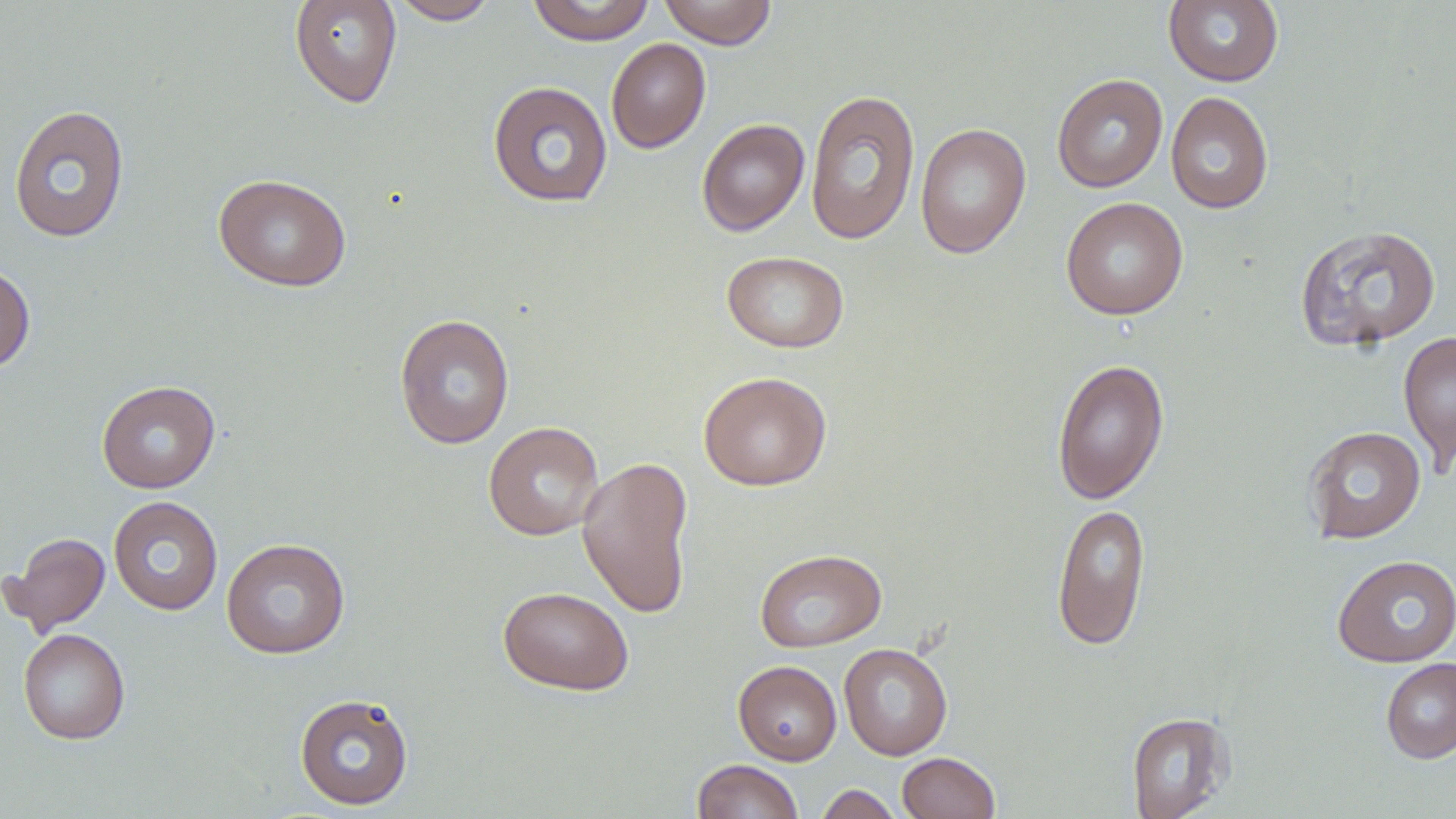 Approximate bounding boxes as (x1,y1)-(x2,y2) corner pairs in pixels. Uninfected red blood cell locations: (288,0)-(402,109), (387,0)-(500,25), (526,0)-(656,45), (658,0)-(778,49), (1163,0)-(1284,87), (606,38)-(711,153), (1051,73)-(1168,193), (487,80)-(613,207), (805,89)-(921,245), (1166,92)-(1274,214), (8,104)-(131,243), (696,119)-(810,236), (915,122)-(1032,259), (213,173)-(351,292), (1060,197)-(1189,320), (1294,224)-(1442,353), (722,250)-(849,353), (0,263)-(36,373), (394,313)-(515,449), (1398,331)-(1456,469), (1051,357)-(1169,505), (698,371)-(831,491), (96,379)-(220,493), (483,421)-(604,540), (1303,425)-(1426,544), (577,455)-(695,620), (108,496)-(224,615), (1052,502)-(1150,651), (3,531)-(110,637), (221,538)-(350,659), (754,548)-(886,653), (1332,554)-(1456,667), (498,586)-(634,695), (18,628)-(130,745), (839,643)-(953,760), (1380,657)-(1456,764), (733,660)-(842,765), (294,692)-(414,811), (1126,711)-(1234,819), (897,752)-(1000,819), (691,760)-(804,819), (816,784)-(902,819). Slide-level diagnosis: negative for blood parasites. Image is 1456×819 pixels. May-Grünwald-Giemsa-stained preparation. Thin blood smear. 1000x magnification. Light microscopy. One field of a larger specimen.